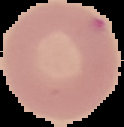 The area outside the segmented cell region is set to black. Image is 124×127 pixels. From a thin blood film. Malaria status: uninfected.